State which parasite is depicted.
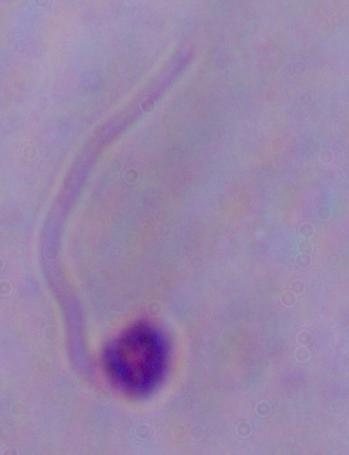

Leishmania.

Summary:
  - Magnification: 1000x
  - Modality: photomicrograph